Report the malaria status of this cell.
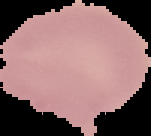
It is uninfected.

From a thin blood film. Cell region segmented out of the field of view; the surrounding area is masked to black. Image is 151×136 pixels.